Report the malaria status of this cell.
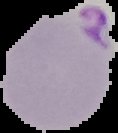
It is parasitized.

Summary:
  - Image size: 118×133 pixels
  - Image type: segmented cell region with the area outside set to black
  - Preparation: thin blood film